Classify this cell by malaria status.
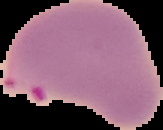

It is parasitized.

Summary:
  - Preparation: thin blood smear
  - Image size: 163×130 pixels
  - Image type: segmented cell region with the area outside set to black